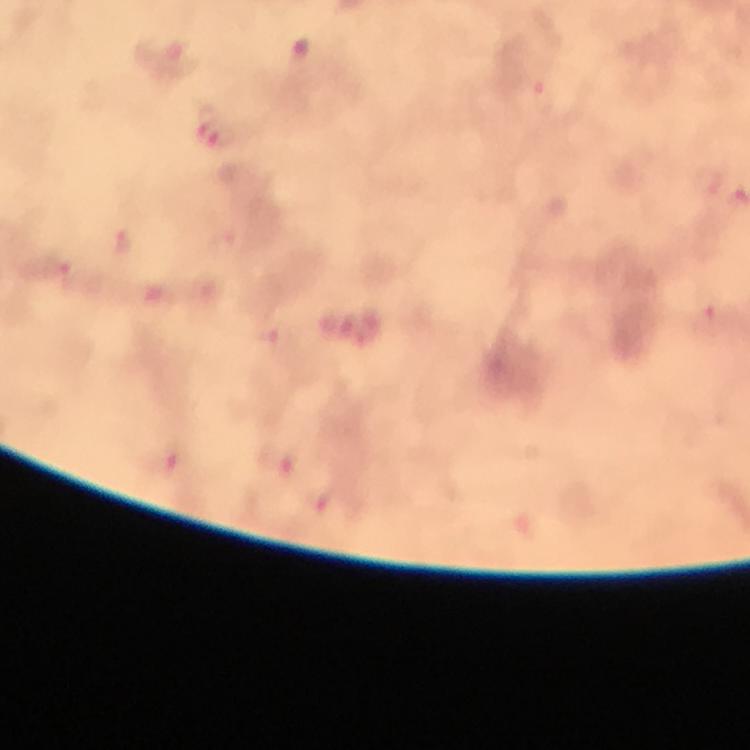

stain = Giemsa
context = from a diagnostic examination for malaria
image size = 750×750 pixels
immersion oil = used
preparation = thick blood smear
cropped from = one field of view
magnification = 100x
capture = smartphone mounted on the microscope
malaria parasite locations = approximate centers as {x, y} in pixels: {202, 122}, {223, 137}